State the blood parasite species.
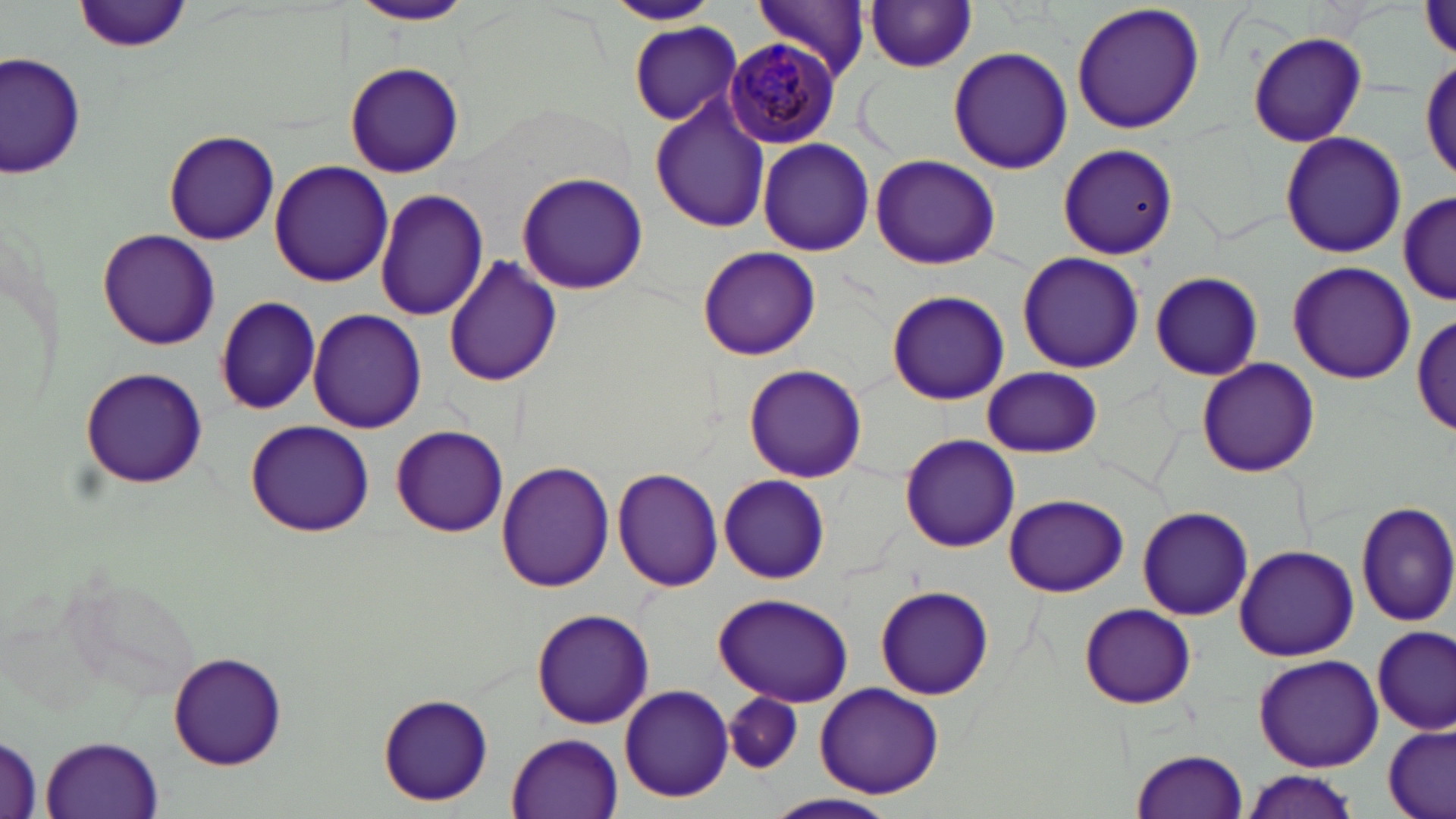
Plasmodium malariae.

preparation = thin blood smear
stain = May-Grünwald-Giemsa
field of view = one of a larger specimen
magnification = 1000x
uninfected red blood cell locations = approximate bounding boxes as (x1,y1)-(x2,y2) corner pairs in pixels: (349,0)-(476,27), (604,0)-(722,26), (751,0)-(871,80), (76,1)-(192,55), (863,2)-(979,73), (1070,2)-(1206,137), (629,22)-(742,125), (1248,30)-(1367,149), (947,46)-(1073,175), (2,50)-(83,176), (1419,55)-(1454,191), (343,61)-(465,178), (650,96)-(771,232), (163,131)-(280,245), (1279,131)-(1408,258), (756,138)-(875,256), (1057,144)-(1177,259), (868,154)-(1002,270), (269,160)-(394,287), (515,171)-(649,295), (374,189)-(488,322), (1398,189)-(1452,307), (97,228)-(221,351), (697,244)-(821,360), (1016,249)-(1144,375), (444,258)-(562,389), (1288,263)-(1417,385), (1150,271)-(1263,381), (885,289)-(1011,406), (213,295)-(322,414), (307,309)-(427,433), (1413,314)-(1455,439), (1195,357)-(1321,477), (743,363)-(868,483), (79,366)-(209,489), (982,367)-(1103,458), (244,420)-(374,537), (390,426)-(508,537), (898,432)-(1020,552), (497,462)-(614,592), (611,468)-(723,591), (717,474)-(830,583), (1004,493)-(1127,597), (1354,501)-(1456,629), (1136,507)-(1254,620), (1234,544)-(1359,662), (874,586)-(993,699), (714,593)-(855,706), (1079,604)-(1196,709), (530,608)-(655,729), (1374,624)-(1454,734), (167,654)-(287,768), (1252,654)-(1384,769), (814,682)-(945,798), (618,683)-(736,802), (378,692)-(493,808), (726,692)-(803,774), (1384,723)-(1454,819), (507,732)-(622,817), (0,735)-(41,817), (42,735)-(164,817), (1130,749)-(1249,818), (1238,771)-(1362,818), (764,792)-(901,819)
image size = 1456×819 pixels
modality = optical microscopy
Plasmodium malariae-infected red blood cell locations = approximate bounding boxes as (x1,y1)-(x2,y2) corner pairs in pixels: (725,37)-(844,145)